Name the parasite shown.
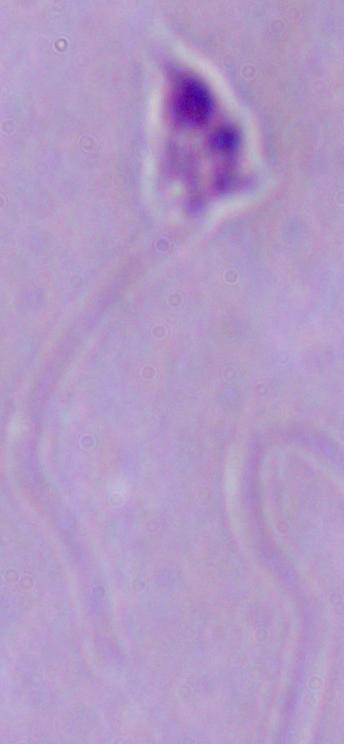
This is Leishmania.

1000x magnification. Micrograph.